Report the malaria status of this cell.
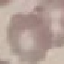
Uninfected.

Cell patch, automatically extracted from a larger field of view and resized to 64 × 64 pixels. Thin smear of blood. Giemsa-stained preparation. Photographed with a smartphone camera at the microscope eyepiece.